Classify this cell by malaria status.
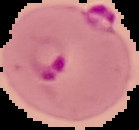

Parasitized.

Summary:
  - Image size: 139×130 pixels
  - Preparation: thin blood smear
  - Image type: cell region segmented out of the field of view; surrounding area masked to black